Outline platelets.
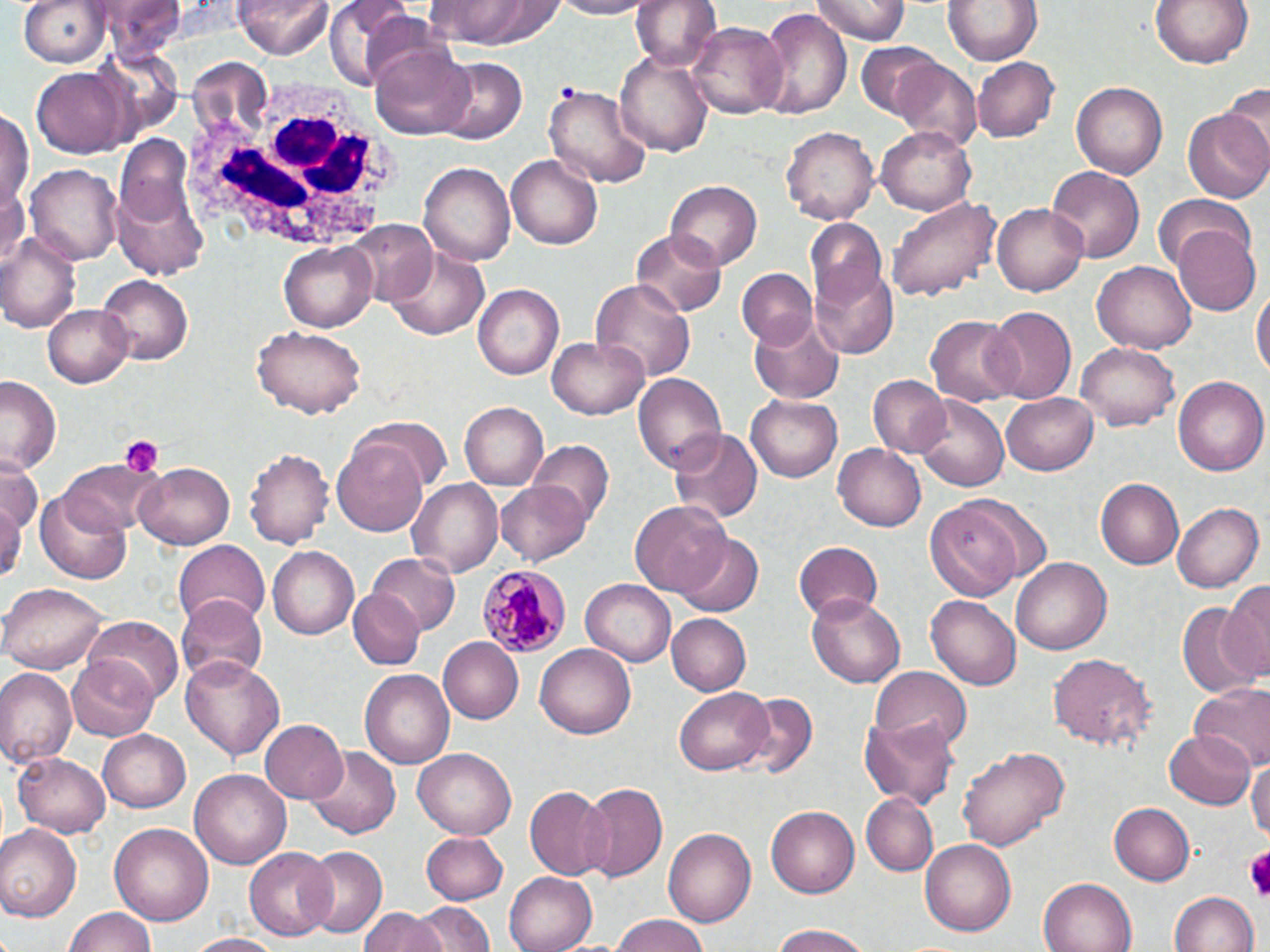

Approximate bounding boxes as (x1, y1, x2, y2) in pixels.
Platelets: (118, 435, 163, 479), (1249, 847, 1270, 903).

Summary:
  - White blood cell locations: (180, 70, 408, 256)
  - Plasmodium malariae-infected red blood cell locations: (476, 562, 568, 656)
  - Uninfected red blood cell locations: (18, 0, 111, 68), (89, 0, 188, 57), (235, 0, 331, 60), (423, 0, 565, 47), (544, 0, 655, 18), (631, 0, 720, 76), (813, 0, 907, 47), (945, 0, 1042, 66), (1148, 0, 1258, 70), (325, 2, 423, 89), (755, 7, 851, 119), (688, 21, 788, 120), (368, 42, 476, 141), (854, 42, 942, 121), (615, 49, 714, 157), (438, 56, 525, 142), (973, 57, 1059, 142), (888, 60, 981, 150), (31, 68, 131, 157), (1071, 80, 1167, 179), (1222, 80, 1270, 165), (546, 82, 647, 188), (1183, 106, 1270, 204), (0, 110, 32, 215), (877, 125, 978, 215), (781, 126, 879, 226), (115, 136, 195, 227), (507, 153, 604, 249), (419, 162, 515, 267), (26, 164, 123, 266), (1046, 167, 1145, 261), (667, 179, 763, 271), (111, 182, 210, 278), (0, 186, 27, 271), (887, 195, 1000, 303), (1151, 196, 1252, 271), (991, 204, 1089, 296), (347, 220, 438, 305), (804, 220, 889, 311), (1172, 224, 1259, 315), (630, 228, 727, 316), (0, 229, 82, 335), (385, 241, 491, 340), (280, 242, 376, 333), (1091, 262, 1197, 354), (809, 264, 900, 358), (736, 270, 814, 348), (98, 276, 195, 365), (591, 277, 696, 388), (472, 284, 562, 380), (1253, 285, 1269, 378), (44, 305, 133, 388), (983, 305, 1077, 404), (749, 310, 846, 405), (927, 315, 1020, 406), (250, 326, 366, 418), (547, 337, 650, 421), (1075, 342, 1179, 432), (634, 371, 728, 476), (1172, 375, 1268, 477), (869, 376, 950, 459), (1, 377, 62, 474), (746, 393, 848, 482), (1002, 394, 1099, 478), (914, 395, 1009, 492), (459, 402, 548, 489), (357, 417, 452, 494), (668, 428, 763, 524), (331, 436, 431, 537), (528, 441, 613, 527), (833, 442, 927, 533), (244, 446, 333, 550), (59, 459, 157, 536), (0, 461, 41, 536), (135, 461, 234, 548), (406, 476, 503, 575), (1096, 479, 1185, 569), (498, 480, 590, 564), (0, 489, 24, 584), (37, 493, 131, 584), (927, 498, 1025, 602), (632, 500, 733, 597), (1171, 502, 1261, 593), (679, 534, 764, 617), (172, 540, 269, 627), (792, 540, 884, 623), (267, 545, 361, 640), (367, 552, 459, 636), (1013, 557, 1112, 654), (580, 578, 676, 667), (1221, 580, 1270, 683), (2, 581, 110, 672), (347, 589, 425, 670), (807, 592, 908, 686), (174, 594, 270, 687), (928, 596, 1020, 691), (1176, 602, 1258, 698), (665, 613, 750, 696), (83, 616, 183, 706), (437, 636, 525, 723), (536, 643, 638, 739), (1050, 652, 1155, 750), (180, 654, 284, 761), (67, 658, 160, 741), (0, 666, 75, 769), (869, 666, 971, 754), (360, 670, 454, 768), (1189, 684, 1270, 772), (674, 688, 773, 774), (736, 693, 816, 779), (859, 716, 959, 807), (260, 719, 349, 804), (97, 729, 191, 813), (1164, 730, 1257, 810), (958, 744, 1071, 851), (307, 746, 400, 840), (414, 748, 517, 838), (14, 750, 113, 838), (1247, 756, 1270, 850), (192, 768, 289, 869), (578, 781, 668, 882), (524, 786, 615, 880), (860, 793, 938, 878), (1108, 802, 1194, 885), (766, 804, 860, 897), (110, 822, 214, 926), (0, 824, 81, 920), (662, 827, 755, 929), (421, 831, 508, 903), (920, 839, 1019, 937), (245, 847, 335, 940), (299, 847, 387, 939), (502, 871, 596, 952), (1038, 877, 1135, 952), (1170, 891, 1260, 952), (414, 900, 495, 952), (65, 908, 158, 952), (360, 909, 439, 952), (607, 916, 715, 952), (765, 921, 875, 952), (183, 933, 285, 952)
  - Slide-level diagnosis: Plasmodium malariae
  - Image size: 1270×952 pixels
  - Magnification: 1000x
  - Stain: May-Grünwald-Giemsa
  - Field of view: single
  - Modality: light microscopy
  - Preparation: thin blood smear